Locate and identify every blood parasite.
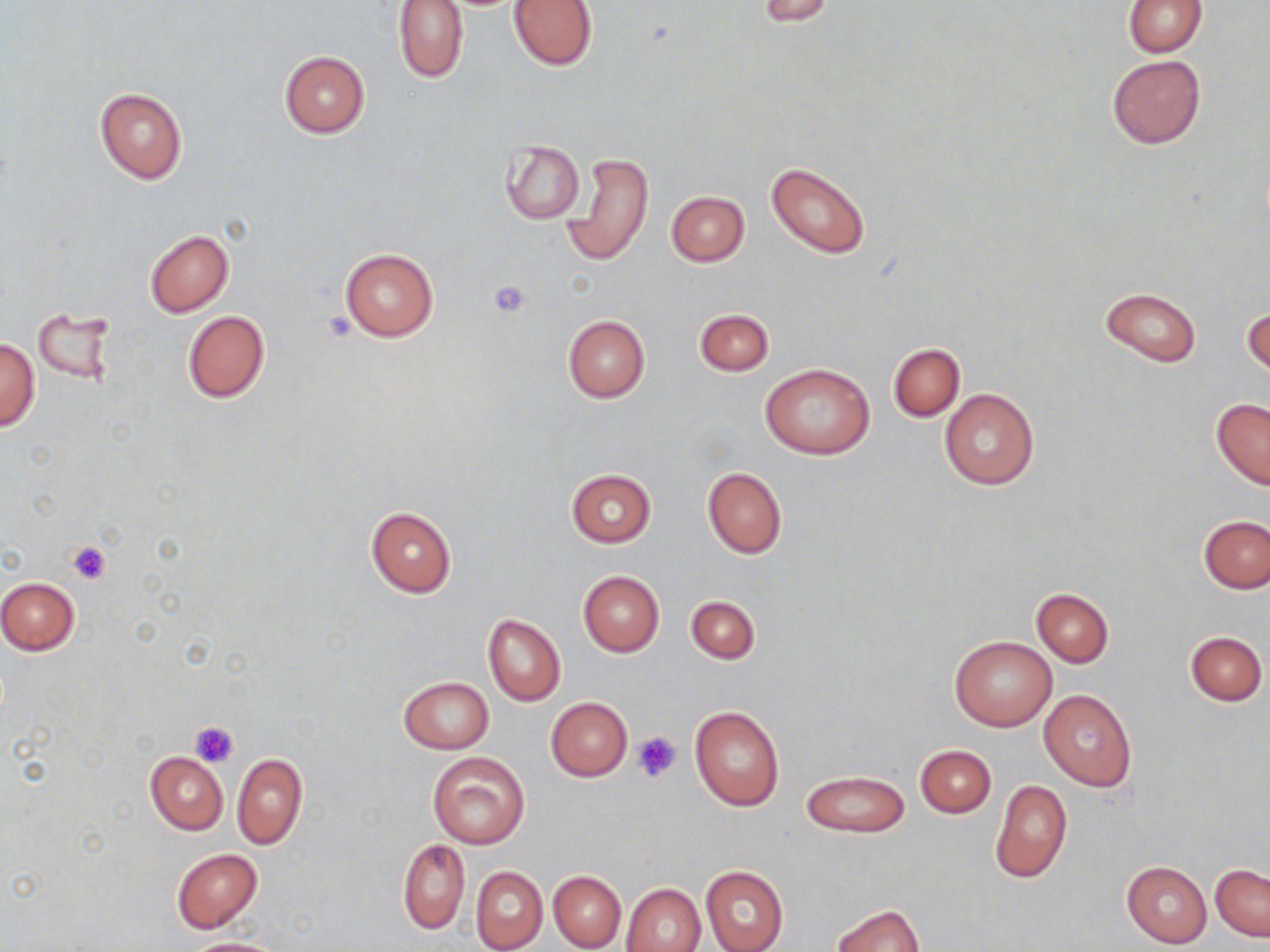

No blood parasites observed.

slide_level_diagnosis: negative for blood parasites
platelet_locations: 'approximate bounding boxes as (x1,y1)-(x2,y2) corner pairs in pixels: (487,278)-(533,319), (67,540)-(112,585), (189,720)-(239,767), (634,731)-(681,780)'
field_of_view: single
uninfected_red_blood_cell_locations: 'approximate bounding boxes as (x1,y1)-(x2,y2) corner pairs in pixels: (392,0)-(469,84), (508,0)-(599,70), (759,0)-(837,26), (1123,0)-(1207,57), (279,51)-(370,137), (1107,54)-(1204,149), (94,87)-(186,184), (501,141)-(584,224), (564,151)-(653,268), (766,162)-(872,259), (665,190)-(750,266), (145,230)-(234,316), (338,246)-(439,342), (1099,287)-(1202,366), (1243,307)-(1269,379), (694,309)-(773,376), (32,310)-(114,385), (182,310)-(270,405), (562,315)-(650,403), (0,338)-(40,431), (888,343)-(964,421), (760,364)-(875,458), (939,389)-(1039,490), (1211,399)-(1270,490), (702,466)-(787,557), (566,469)-(656,547), (365,505)-(456,598), (1199,514)-(1270,594), (577,570)-(664,656), (0,576)-(80,655), (1031,588)-(1114,666), (685,596)-(759,665), (483,615)-(565,706), (1185,631)-(1267,706), (949,636)-(1056,732), (398,675)-(493,754), (1038,687)-(1137,792), (545,697)-(632,781), (690,705)-(784,810), (915,745)-(996,818), (428,751)-(530,850), (145,752)-(227,834), (232,752)-(307,849), (800,771)-(909,837), (989,778)-(1073,883), (398,839)-(469,934), (171,849)-(263,933), (1122,861)-(1212,949), (1210,863)-(1269,941), (472,866)-(548,952), (699,866)-(788,952), (549,872)-(625,951), (622,882)-(705,952), (831,903)-(925,952), (179,938)-(287,952)'
image_size: 1270×952 pixels
stain: May-Grünwald-Giemsa
preparation: thin blood smear
magnification: 1000x
modality: optical microscopy